Draw a bounding box around every artifact (platelet-like body, stain precipitate, or debris).
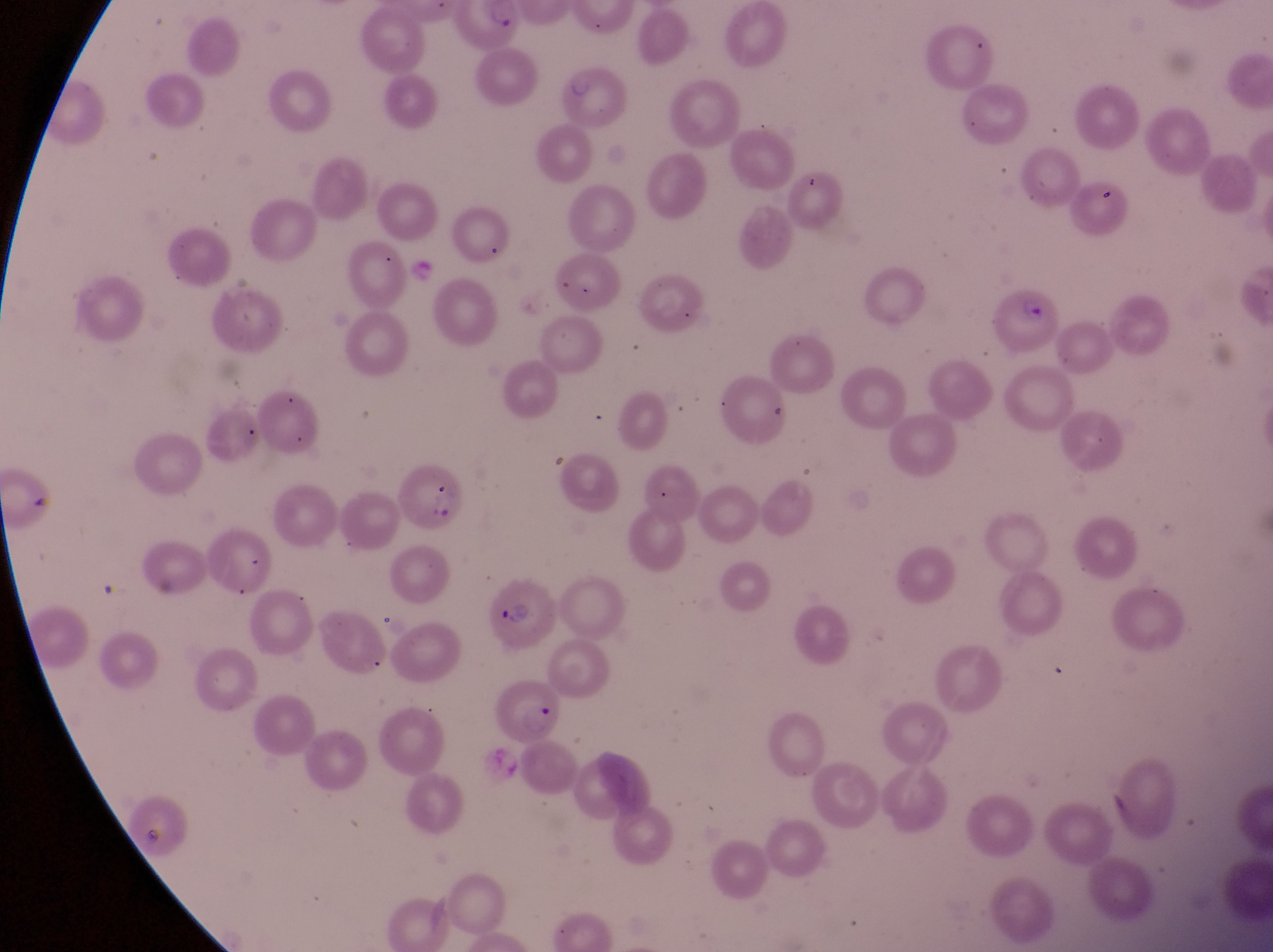

Approximate bounding boxes as (left, top, right, bottom) in pixels.
Artifacts (platelet-like body, stain precipitate, or debris): (137, 816, 169, 855).

capture = smartphone photograph through the eyepiece of an Olympus CX-23 microscope
preparation = thin blood film
parasitised red blood cell locations = approximate bounding boxes as (left, top, right, bottom) in pixels: (458, 1, 523, 54), (983, 278, 1060, 356), (399, 462, 469, 530), (486, 577, 560, 655), (495, 681, 567, 746)
image size = 1273×952 pixels
magnification = 1000x
field of view = single
country = Uganda